State the preparation type.
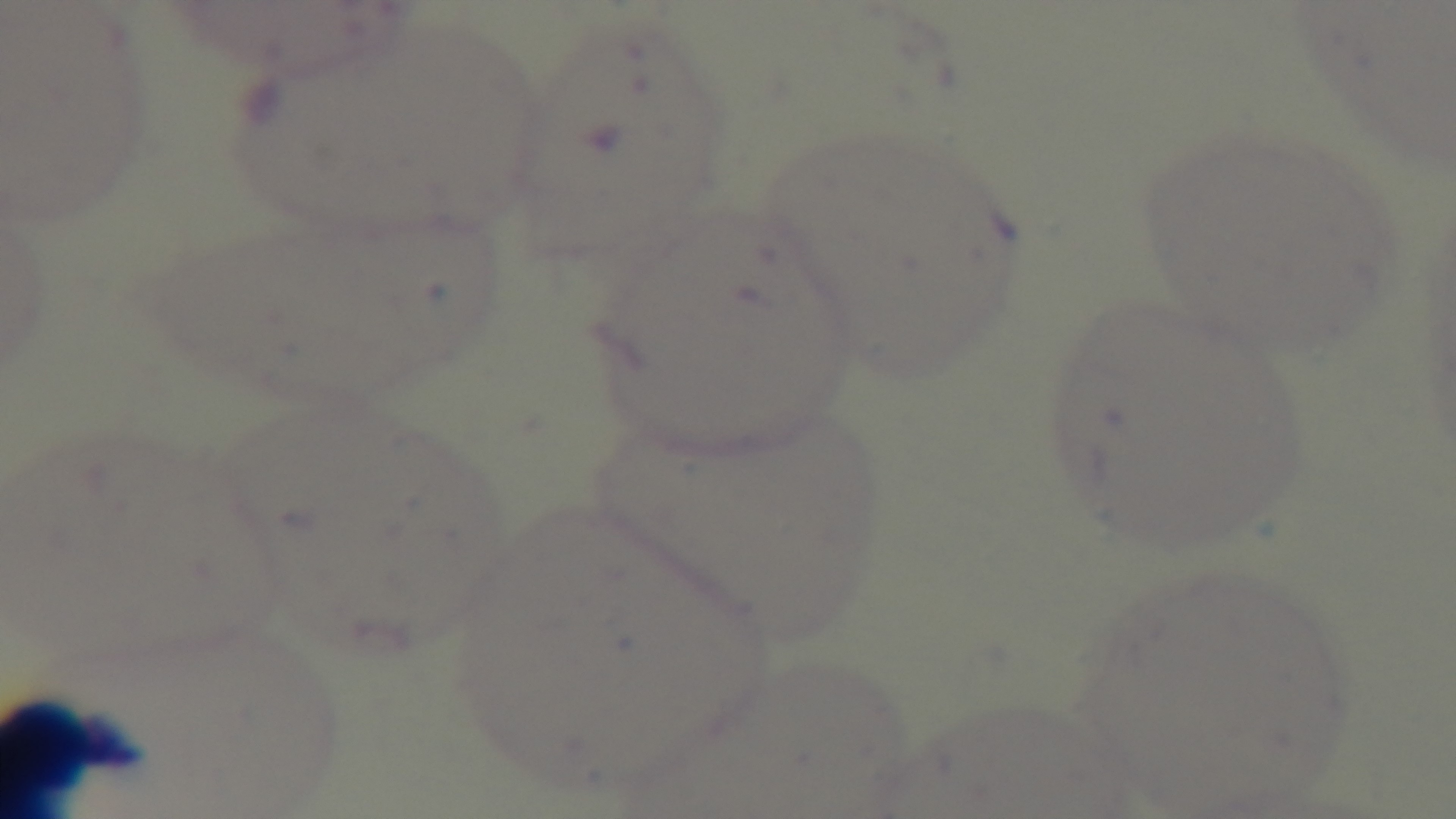

It is a thin blood film.

Malaria status: uninfected. Giemsa stain. Mounted 4K digital camera. 100x oil-immersion objective. Single field of view. Photomicrograph.